State which parasite is depicted.
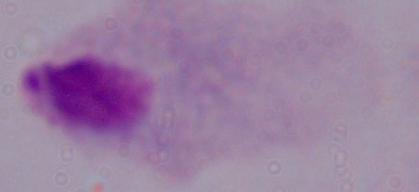

A trichomonad.

modality: photomicrograph
magnification: 1000x